Assess the morphology of the red blood cells.
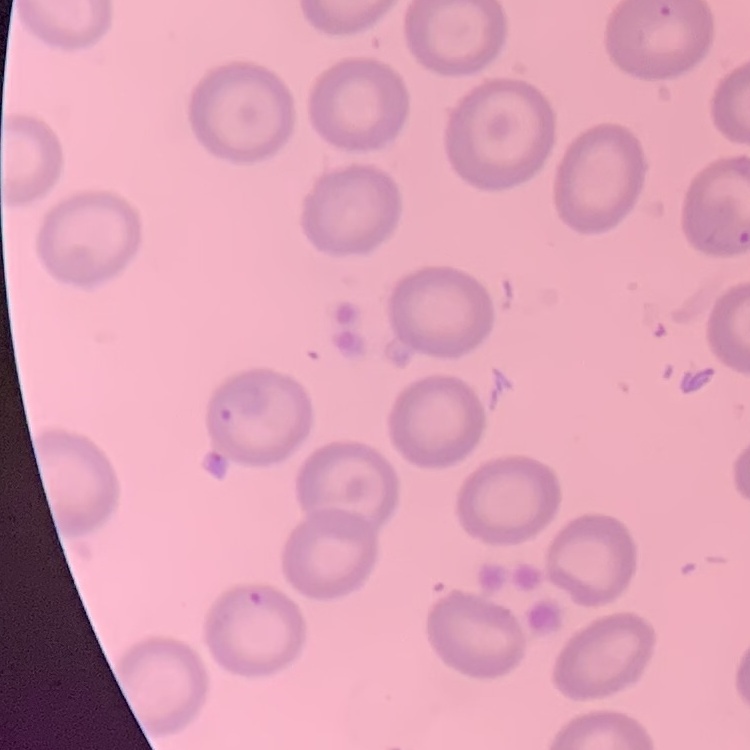
They show no rouleaux formation.

Thin blood smear. Field's or Giemsa stain. Square crop of a larger photomicrograph.